Identify the preparation type.
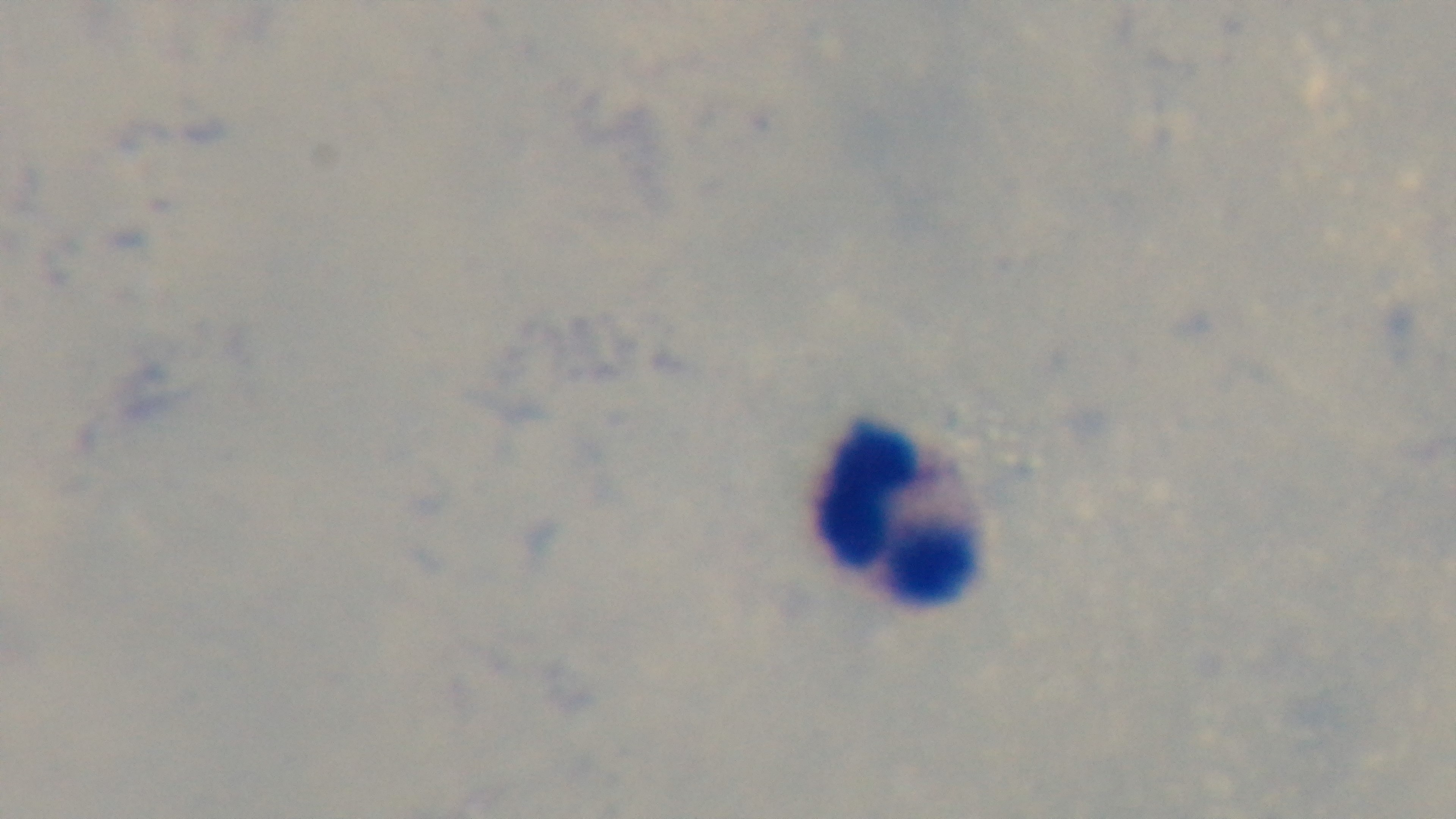
It is a thick blood film.

{
  "modality": "light microscopy",
  "capture": "mounted 4K digital camera",
  "field_of_view": "one from the slide",
  "objective": "100x oil immersion",
  "malaria_status": "uninfected",
  "stain": "Giemsa"
}